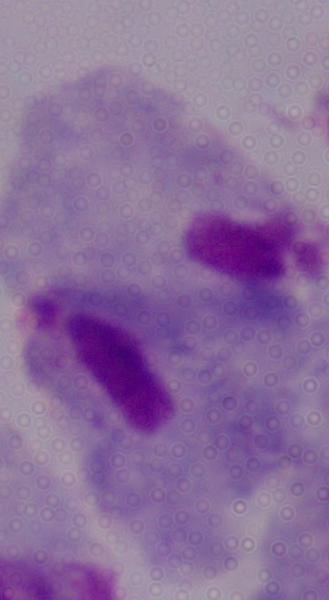
Summary:
  - Identification: trichomonad
  - Magnification: 1000x
  - Modality: micrograph